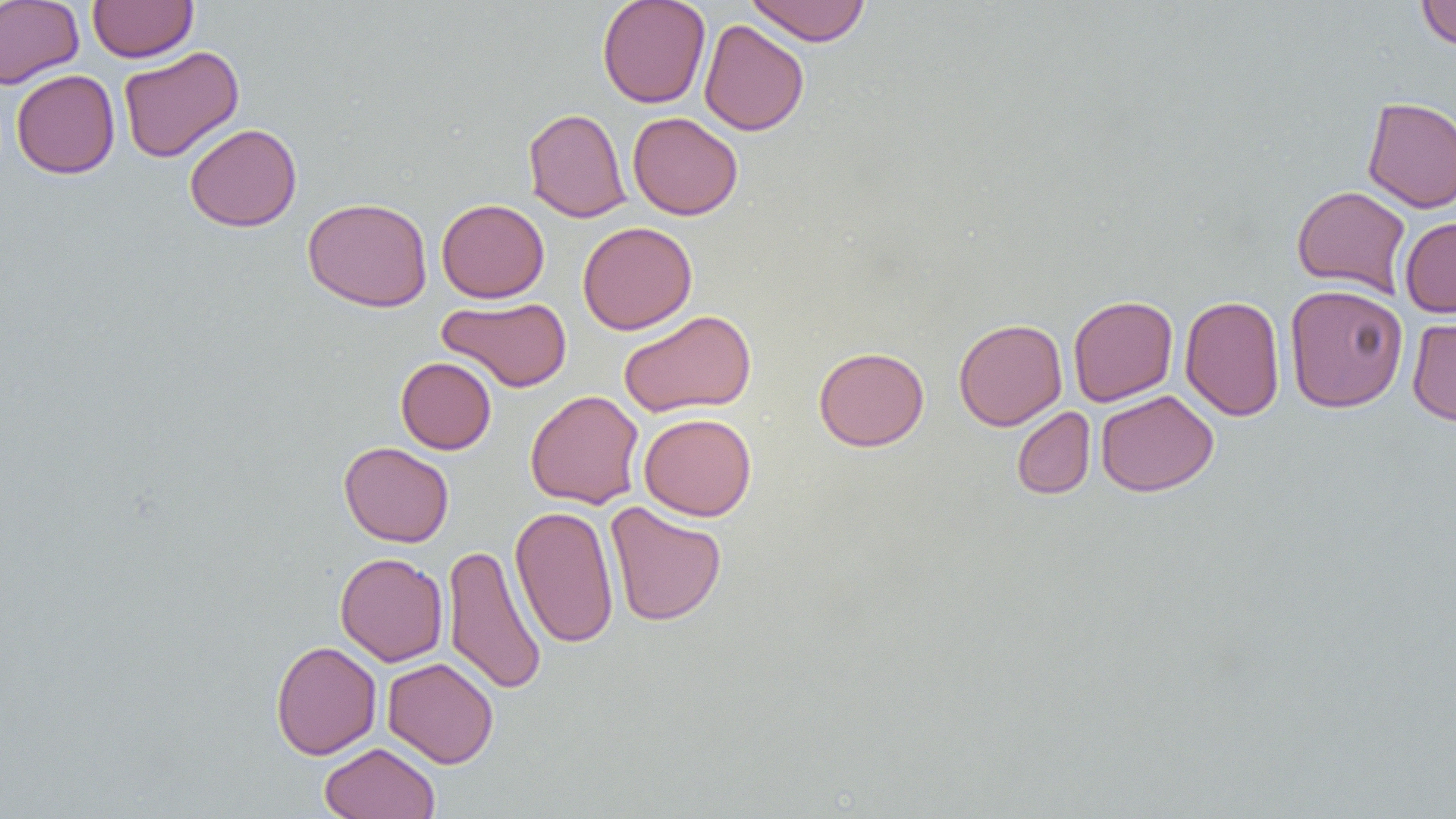
Summary:
  - Coordinate format: approximate bounding boxes as (x1, y1, x2, y2) in pixels
  - Uninfected red blood cell locations: (0, 0, 84, 88), (88, 0, 197, 62), (597, 0, 711, 109), (745, 0, 871, 45), (1416, 0, 1456, 50), (699, 19, 809, 136), (118, 46, 244, 163), (11, 69, 120, 179), (1362, 96, 1456, 212), (523, 107, 632, 223), (627, 112, 743, 220), (184, 123, 302, 232), (1292, 184, 1411, 298), (302, 196, 433, 312), (436, 198, 549, 303), (1399, 217, 1456, 317), (577, 221, 697, 335), (1284, 284, 1408, 413), (1068, 295, 1178, 406), (1179, 295, 1285, 421), (437, 296, 573, 393), (619, 309, 756, 417), (1406, 315, 1456, 426), (953, 318, 1067, 431), (813, 346, 929, 451), (396, 356, 496, 454), (525, 390, 645, 509), (1096, 390, 1218, 497), (1012, 406, 1095, 500), (639, 413, 756, 521), (339, 441, 454, 547), (605, 501, 727, 626), (509, 505, 620, 649), (441, 543, 547, 696), (335, 552, 448, 666), (270, 640, 382, 760), (382, 657, 499, 769), (320, 742, 439, 819)
  - Slide-level diagnosis: no evidence of blood parasites
  - Modality: optical microscopy
  - Field of view: one of a larger specimen
  - Image size: 1456×819 pixels
  - Magnification: 1000x
  - Preparation: thin blood film